Assess this cell for malaria.
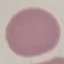
It is uninfected.

Thin blood smear. Acquired by smartphone through the microscope eyepiece. Cell patch, automatically extracted from a larger field of view and resized to 64 × 64 pixels. Giemsa stain.